Assess the morphology of the red blood cells.
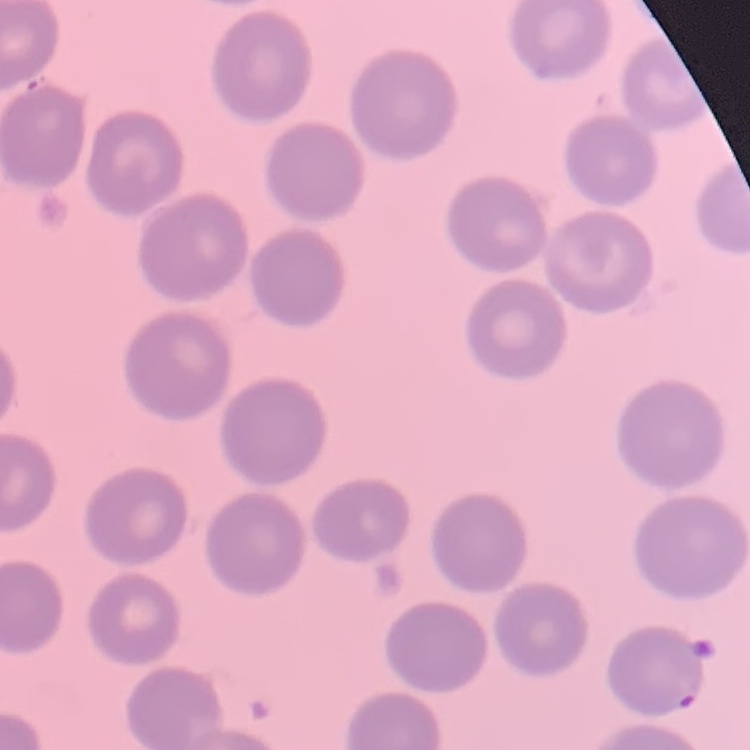
They show no rouleaux formation.

preparation: thin peripheral smear
image_type: square crop of a larger photomicrograph
stain: Field's or Giemsa